State the preparation type.
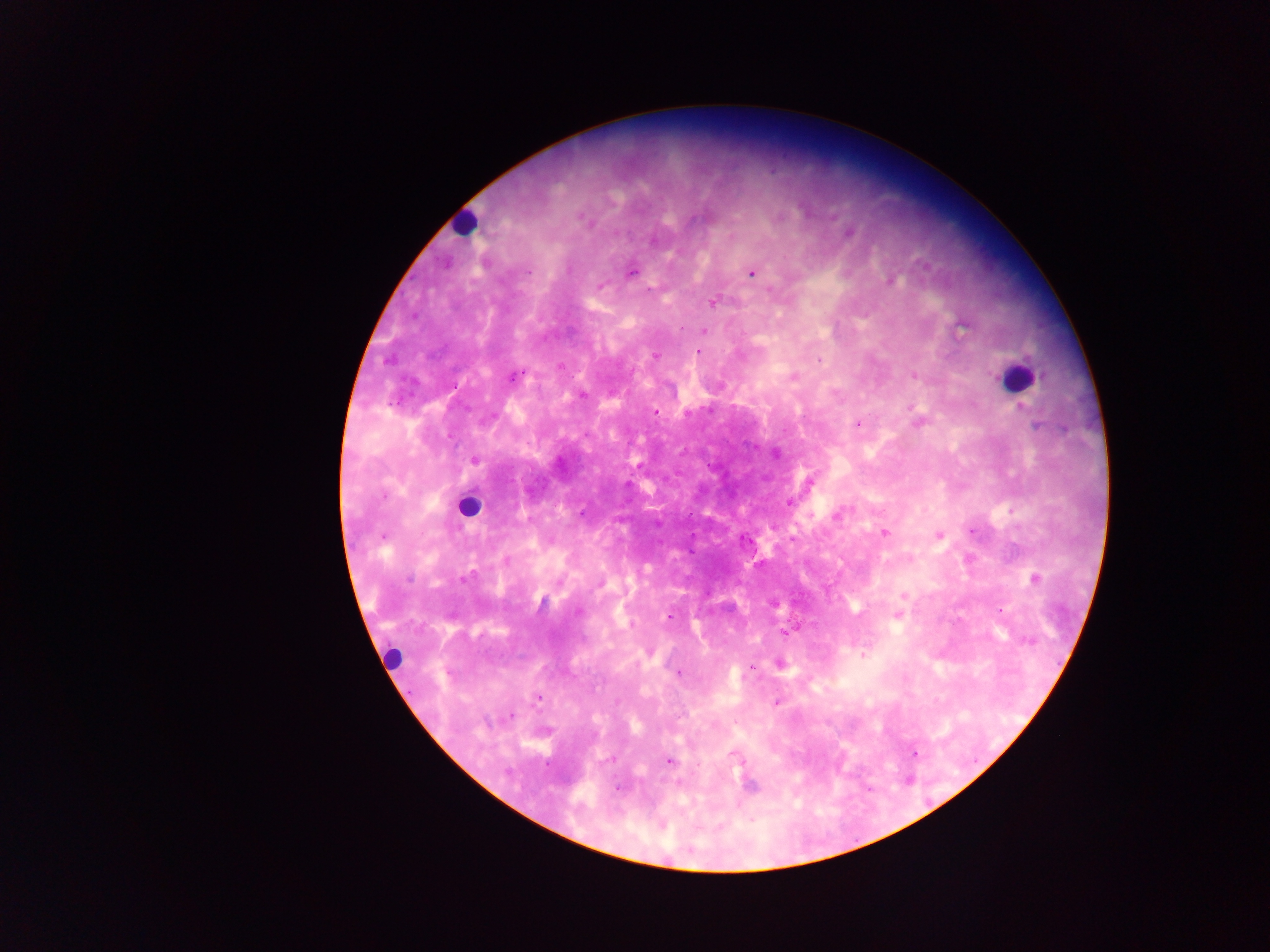
Thick blood smear.

Approximate centers as (x, y) in pixels. Leukocyte locations: (462, 221), (1016, 376), (468, 506), (393, 659). Plasmodium parasite locations: (582, 217), (848, 233), (652, 241), (569, 269), (528, 271), (630, 273), (751, 273), (890, 281), (600, 286), (713, 302), (962, 327), (681, 329), (704, 330), (698, 351), (655, 356), (819, 359), (560, 365), (513, 376), (914, 376), (793, 378), (1023, 409), (656, 411), (914, 412), (687, 414), (1031, 417), (918, 422), (857, 425), (1035, 425), (587, 435), (775, 454), (475, 460), (789, 502), (581, 513), (837, 514), (885, 532), (971, 532), (938, 535), (383, 537), (745, 538), (506, 561), (408, 579), (1034, 579), (462, 580), (904, 595), (900, 607), (1001, 611), (578, 612), (668, 616), (897, 616), (785, 634), (1028, 641), (863, 655), (751, 667), (679, 673), (538, 698), (777, 703), (510, 715), (915, 753), (734, 755), (611, 759), (669, 761), (698, 764), (751, 785), (618, 787), (662, 825). Image is 1270×952 pixels. Mobile-phone photograph taken through the microscope. Single field of view. Collected in Ghana.